Give the position of every Plasmodium parasite visible.
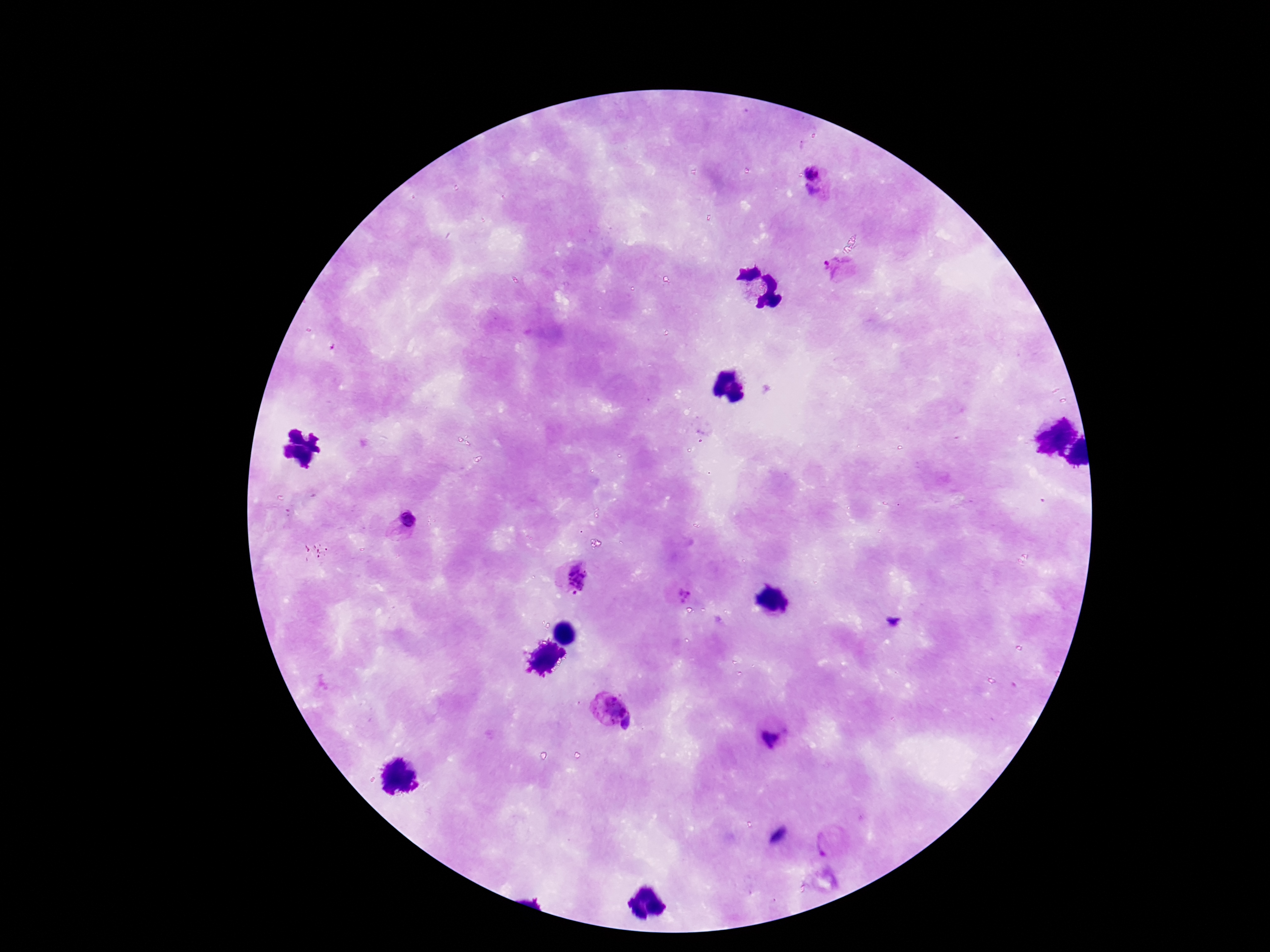

Approximate centers as {x, y} in pixels.
Plasmodium parasites: {812, 171}, {812, 194}, {838, 269}, {408, 521}, {572, 577}, {683, 590}, {609, 706}, {630, 725}, {772, 739}, {829, 843}.

stain = Giemsa
field of view = one from this slide
magnification = 100x
image size = 1270×952 pixels
capture = smartphone camera through the microscope eyepiece
preparation = thick blood film
patient malaria status = infected